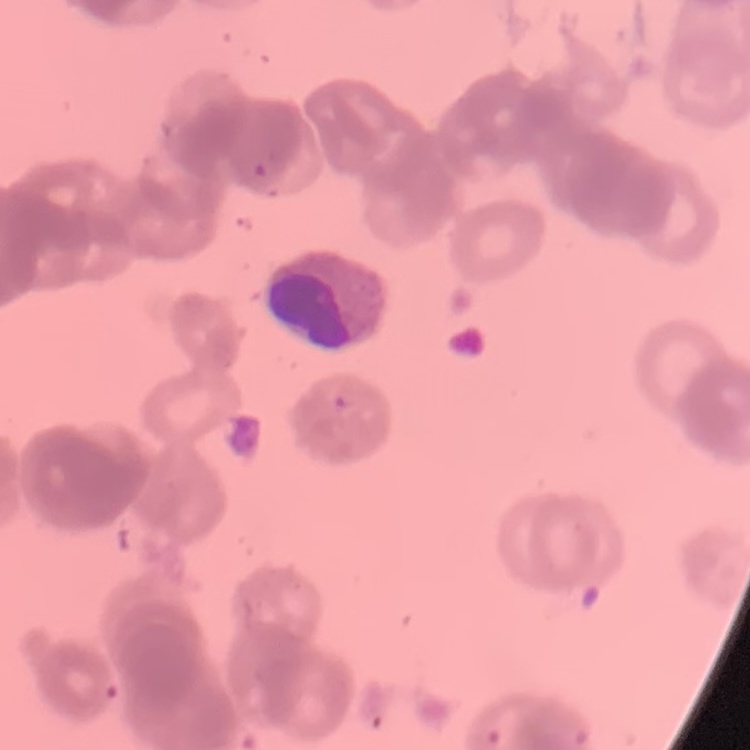

The red blood cells exhibit rouleaux formation. Field's or Giemsa stain. Thin blood smear. Square crop of a larger photomicrograph.